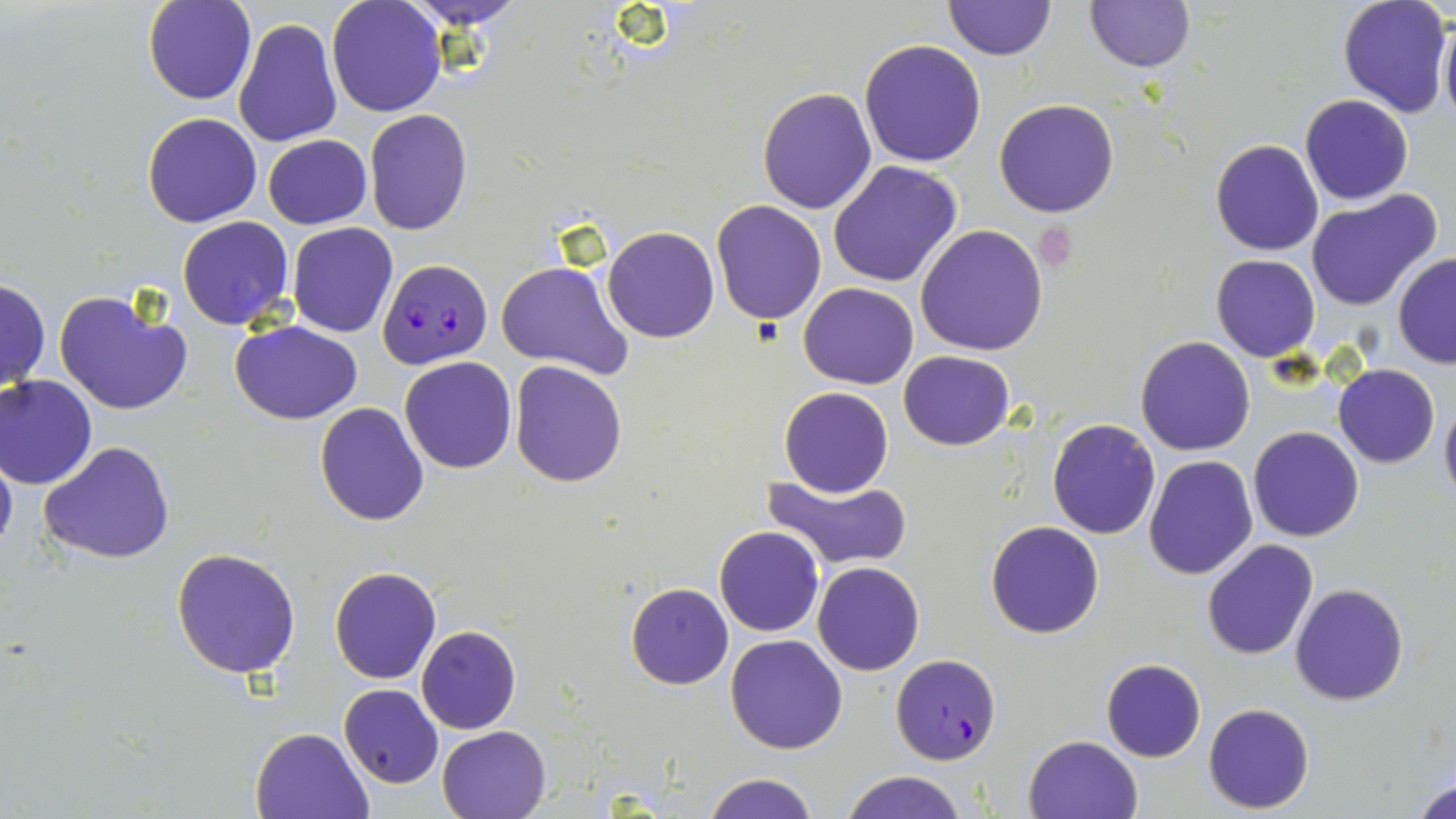

Summary:
  - Coordinate format: approximate bounding boxes as named x1/y1/x2/y2 corners in pixels
  - Platelet locations: (x1=1033, y1=226, x2=1078, y2=267)
  - Uninfected red blood cell locations: (x1=142, y1=0, x2=255, y2=104), (x1=325, y1=0, x2=446, y2=118), (x1=402, y1=0, x2=529, y2=28), (x1=943, y1=0, x2=1054, y2=60), (x1=1337, y1=0, x2=1452, y2=119), (x1=1083, y1=1, x2=1196, y2=73), (x1=1438, y1=16, x2=1456, y2=130), (x1=231, y1=17, x2=342, y2=149), (x1=859, y1=40, x2=987, y2=168), (x1=756, y1=86, x2=878, y2=213), (x1=1299, y1=94, x2=1413, y2=205), (x1=994, y1=98, x2=1121, y2=218), (x1=363, y1=109, x2=473, y2=235), (x1=142, y1=111, x2=263, y2=228), (x1=262, y1=134, x2=372, y2=229), (x1=1211, y1=139, x2=1325, y2=256), (x1=828, y1=160, x2=963, y2=287), (x1=1305, y1=191, x2=1442, y2=311), (x1=710, y1=199, x2=827, y2=325), (x1=177, y1=216, x2=294, y2=331), (x1=287, y1=221, x2=398, y2=338), (x1=915, y1=225, x2=1049, y2=357), (x1=602, y1=227, x2=718, y2=343), (x1=1209, y1=254, x2=1321, y2=362), (x1=1393, y1=254, x2=1456, y2=368), (x1=497, y1=260, x2=634, y2=380), (x1=0, y1=276, x2=50, y2=394), (x1=798, y1=282, x2=918, y2=389), (x1=53, y1=287, x2=192, y2=416), (x1=231, y1=320, x2=363, y2=423), (x1=1135, y1=336, x2=1256, y2=456), (x1=898, y1=349, x2=1016, y2=450), (x1=400, y1=356, x2=518, y2=473), (x1=509, y1=362, x2=628, y2=486), (x1=1334, y1=363, x2=1439, y2=467), (x1=0, y1=374, x2=98, y2=489), (x1=778, y1=387, x2=893, y2=497), (x1=1440, y1=392, x2=1456, y2=508), (x1=315, y1=402, x2=429, y2=525), (x1=1047, y1=418, x2=1160, y2=538), (x1=1247, y1=427, x2=1364, y2=543), (x1=0, y1=441, x2=17, y2=559), (x1=38, y1=441, x2=176, y2=565), (x1=1144, y1=454, x2=1258, y2=580), (x1=763, y1=473, x2=914, y2=571), (x1=986, y1=520, x2=1104, y2=638), (x1=714, y1=525, x2=824, y2=637), (x1=1201, y1=538, x2=1320, y2=659), (x1=172, y1=547, x2=301, y2=679), (x1=812, y1=562, x2=925, y2=676), (x1=330, y1=566, x2=441, y2=684), (x1=625, y1=582, x2=733, y2=688), (x1=1289, y1=582, x2=1410, y2=706), (x1=416, y1=625, x2=521, y2=733), (x1=725, y1=634, x2=849, y2=753), (x1=1099, y1=657, x2=1206, y2=762), (x1=339, y1=684, x2=443, y2=788), (x1=272, y1=699, x2=442, y2=809), (x1=1203, y1=702, x2=1314, y2=814), (x1=437, y1=725, x2=551, y2=818), (x1=250, y1=727, x2=373, y2=818), (x1=1023, y1=734, x2=1144, y2=819), (x1=1412, y1=770, x2=1455, y2=819), (x1=839, y1=771, x2=967, y2=819), (x1=702, y1=773, x2=820, y2=819)
  - Plasmodium falciparum-infected red blood cell locations: (x1=376, y1=256, x2=493, y2=368), (x1=890, y1=653, x2=1002, y2=762)
  - Slide-level diagnosis: Plasmodium falciparum
  - Stain: May-Grünwald-Giemsa
  - Modality: light microscopy
  - Magnification: 1000x
  - Image size: 1456×819 pixels
  - Field of view: single
  - Preparation: thin blood film